State which cell type is depicted.
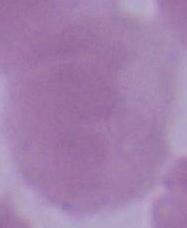

This is an erythrocyte.

modality = photomicrograph
magnification = 1000x